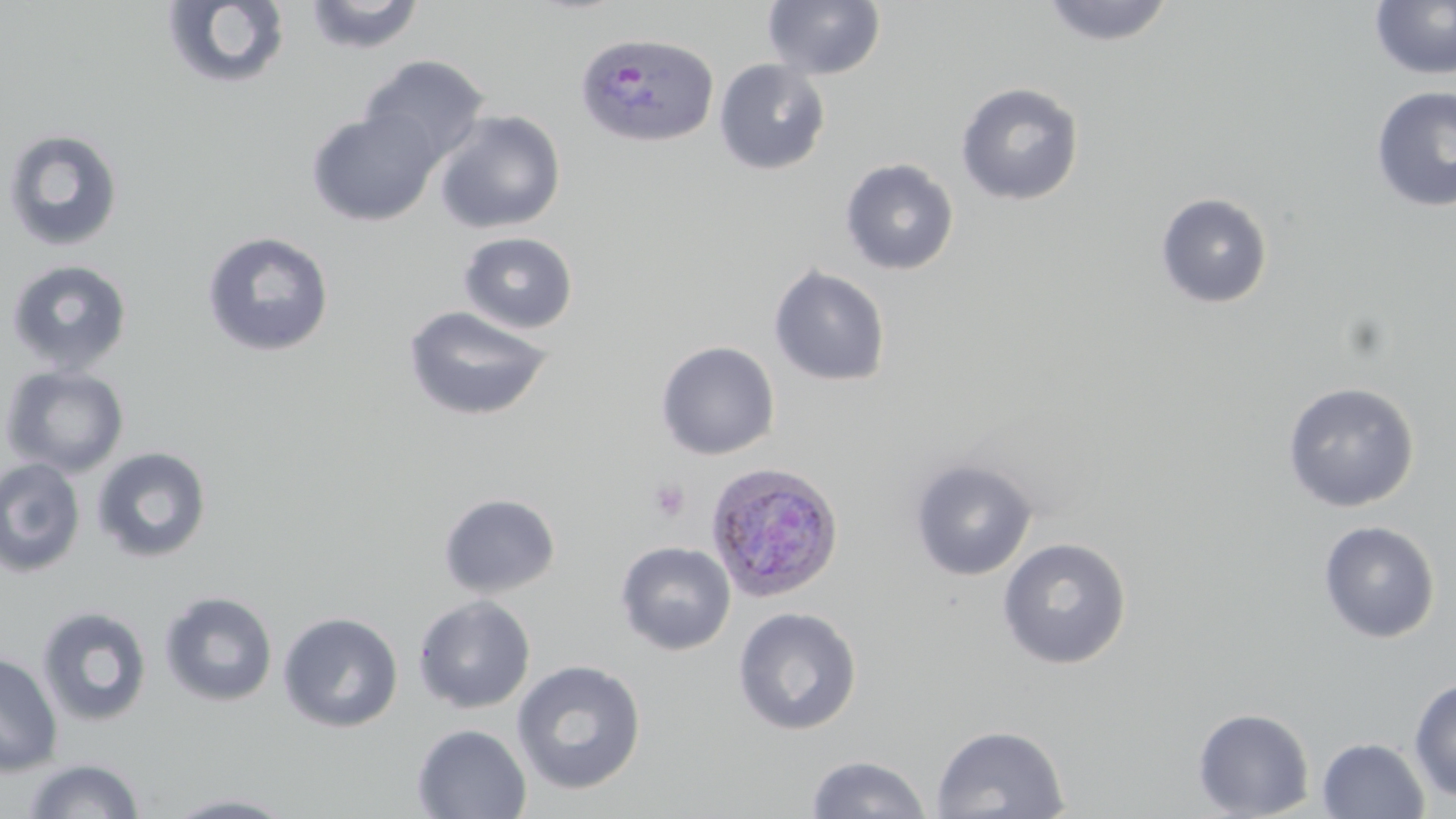

Approximate bounding boxes as (x1,y1)-(x2,y2) corner pairs in pixels. Plasmodium ovale-infected red blood cell locations: (574,31)-(719,148), (705,461)-(845,603). Platelet locations: (648,478)-(691,522). Uninfected red blood cell locations: (160,0)-(292,92), (303,0)-(425,54), (1039,0)-(1175,47), (763,1)-(885,80), (1369,1)-(1456,80), (357,54)-(490,167), (713,59)-(831,176), (955,82)-(1084,206), (1370,85)-(1456,213), (306,108)-(441,226), (434,110)-(566,234), (1,128)-(125,252), (839,158)-(959,275), (1155,192)-(1274,308), (201,231)-(335,358), (457,231)-(579,334), (4,258)-(133,375), (768,265)-(891,387), (403,304)-(555,422), (655,340)-(780,460), (1,364)-(130,478), (1282,381)-(1419,512), (91,447)-(212,564), (0,457)-(86,578), (910,459)-(1038,580), (439,493)-(561,598), (1318,520)-(1440,643), (996,536)-(1132,670), (615,541)-(737,656), (158,591)-(278,708), (412,594)-(536,714), (37,605)-(152,728), (732,606)-(862,735), (278,611)-(404,733), (0,652)-(63,777), (512,659)-(647,795), (1408,676)-(1456,801), (1192,707)-(1314,819), (931,723)-(1069,818), (412,724)-(532,818), (1317,738)-(1430,819), (805,754)-(931,818), (22,758)-(146,818), (161,792)-(299,818). Slide-level diagnosis: Plasmodium ovale. Thin blood smear. Optical microscopy. 1000x magnification. May-Grünwald-Giemsa-stained preparation. Single field of view. Image is 1456×819 pixels.